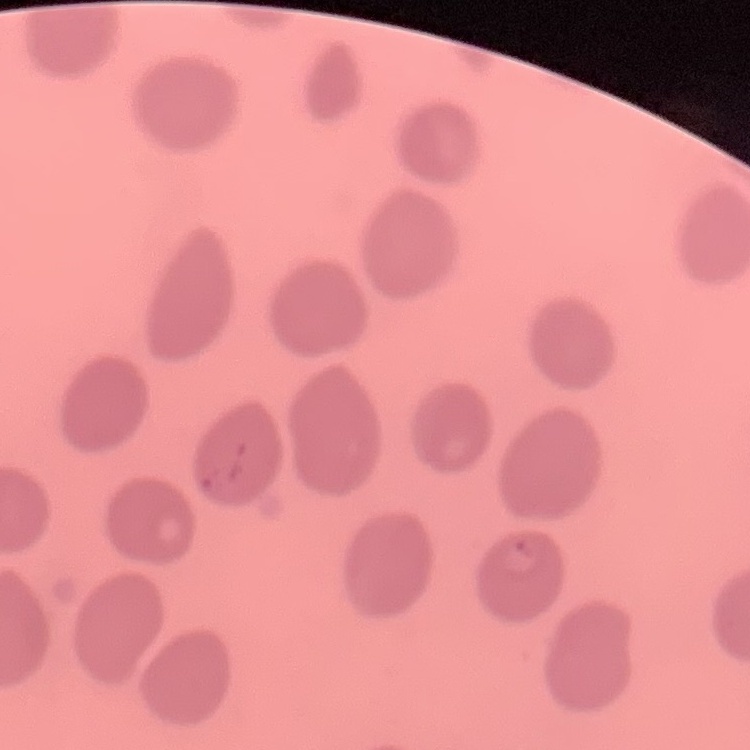
The erythrocytes show no rouleaux formation. Thin blood smear. Stained with either Field's or Giemsa. Square crop of a larger photomicrograph.